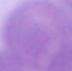 Micrograph. A red blood cell is seen. Captured at 1000x magnification.